Assess for malaria.
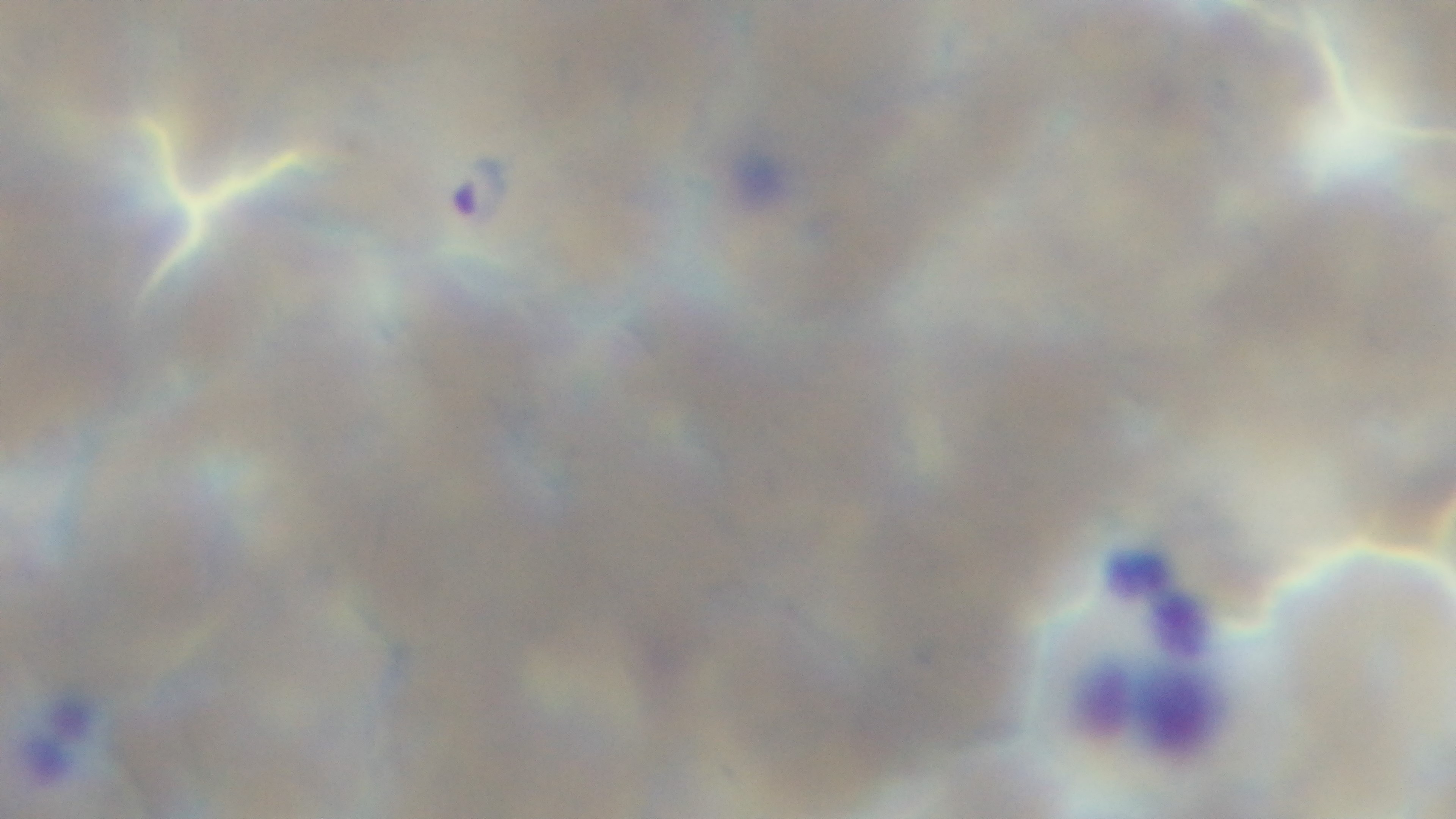
It is infected.

Mounted 4K digital camera. 100x oil-immersion objective. Giemsa-stained. Single field of view. Photomicrograph. Preparation: thin.